Describe the morphology of the erythrocytes.
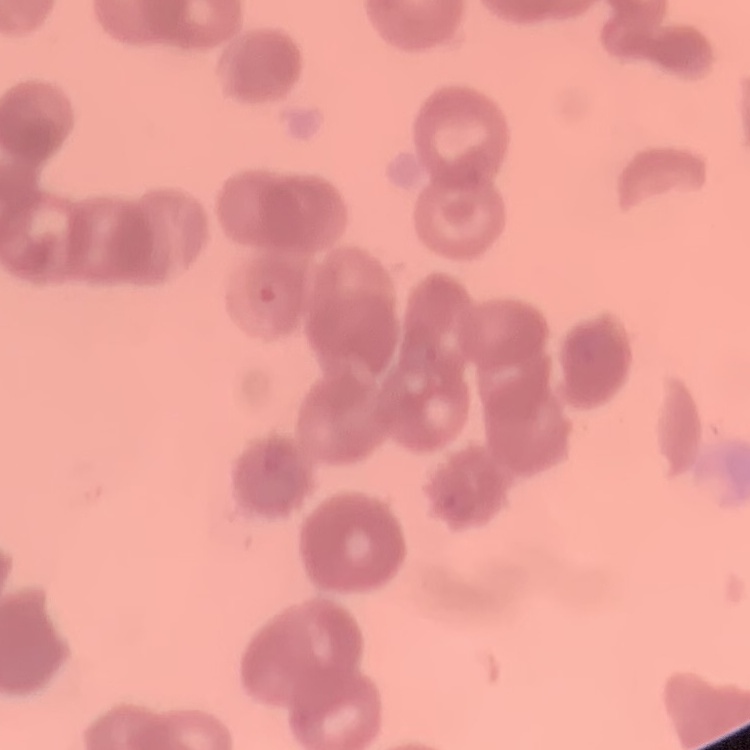

They show rouleaux formation.

image type = square crop of a larger photomicrograph
stain = Field's or Giemsa
preparation = thin peripheral smear